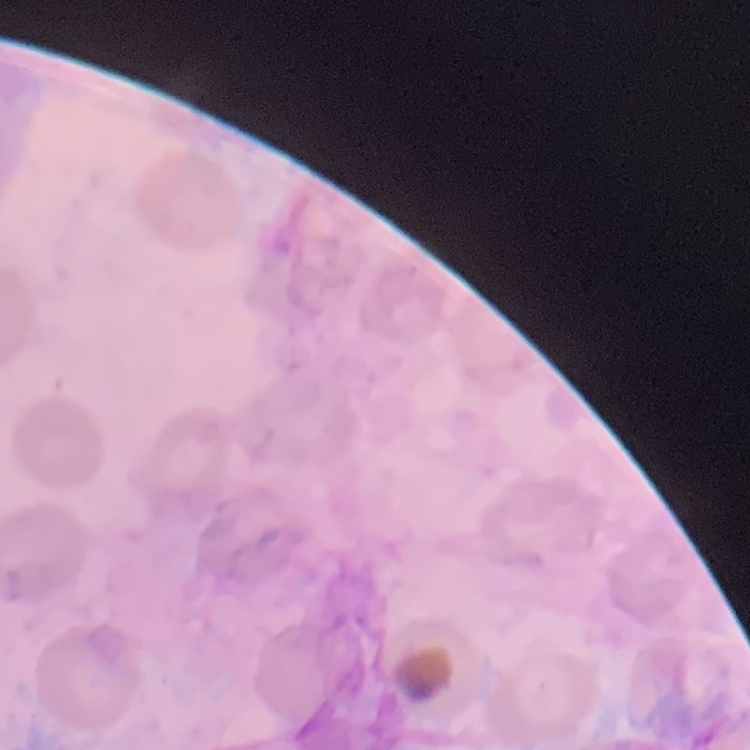
red blood cell morphology = no rouleaux formation
preparation = thin blood film
image type = square crop of a larger photomicrograph
stain = Field's or Giemsa